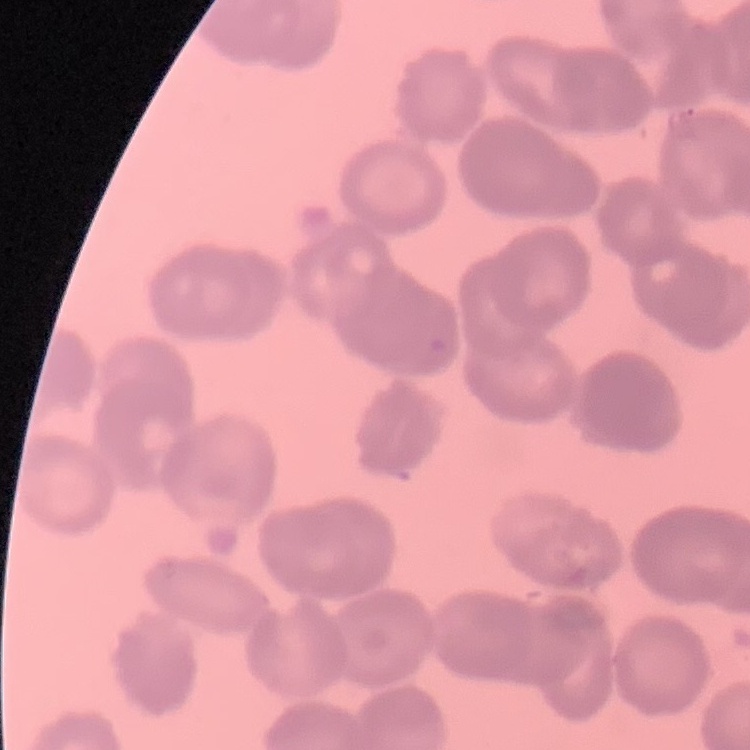 The red blood cells show rouleaux formation. Thin peripheral smear. Square crop of a larger photomicrograph. Field's or Giemsa stain.